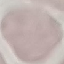

Summary:
  - Result: no malaria parasites seen
  - Preparation: thin smear
  - Stain: Giemsa
  - Image type: cell patch, automatically extracted from a larger field of view and resized to 64 × 64 pixels
  - Capture: smartphone camera at the microscope eyepiece